Assess this cell for malaria.
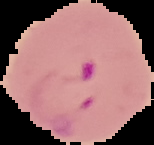

It is parasitized.

preparation: thin blood smear
image_type: segmented cell region with the area outside set to black
image_size: 154×145 pixels